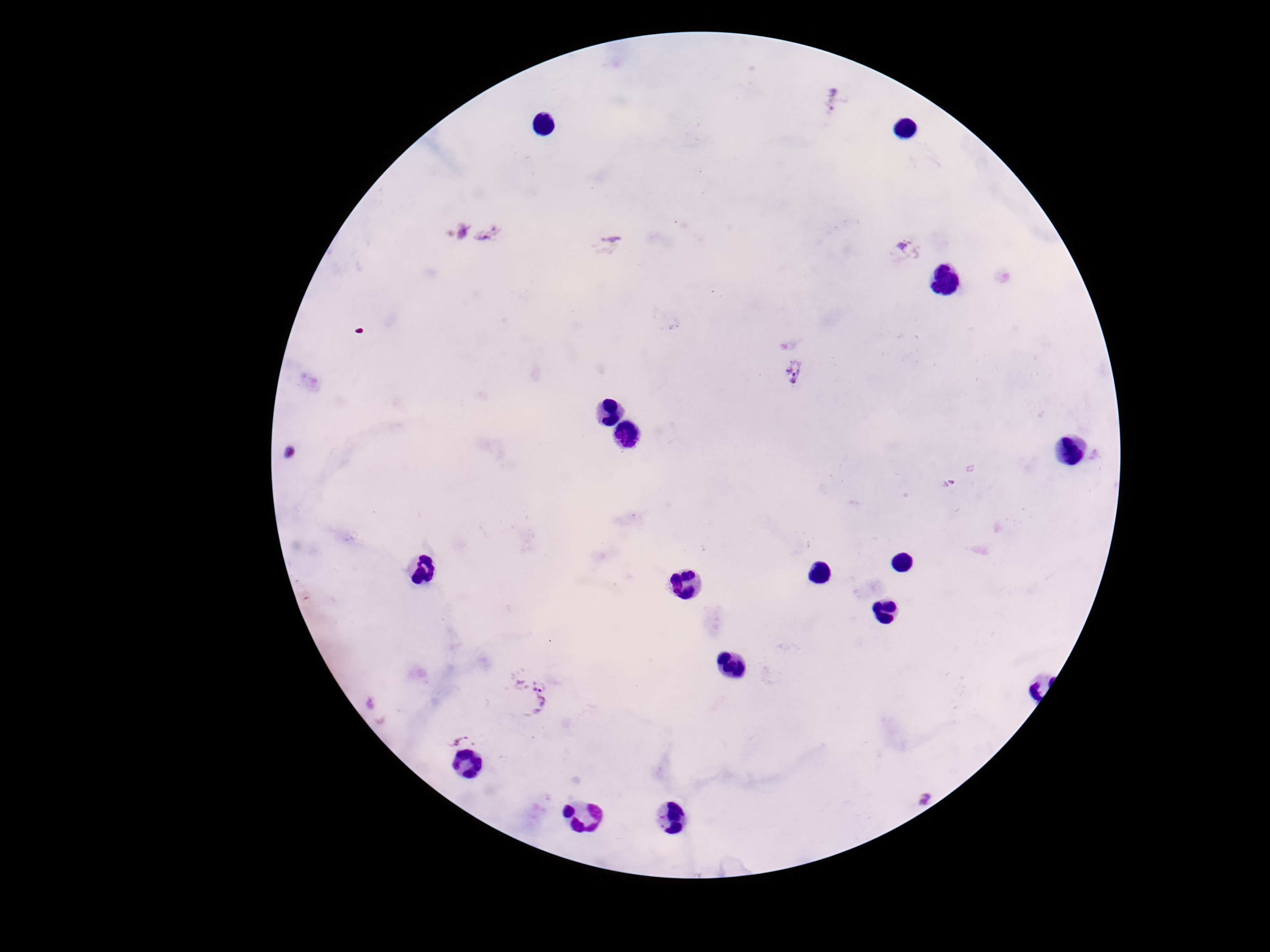
Approximate object centers, in pixels from the top-left corner.
Summary:
  - Plasmodium parasite locations: (x=834, y=103), (x=475, y=231), (x=610, y=245), (x=906, y=247), (x=795, y=372), (x=533, y=697), (x=460, y=740), (x=923, y=794)
  - Patient malaria status: infected
  - Magnification: 100x
  - Stain: Giemsa
  - Field of view: one from this slide
  - Preparation: thick blood smear
  - Capture: smartphone camera through the microscope eyepiece
  - Image size: 1270×952 pixels